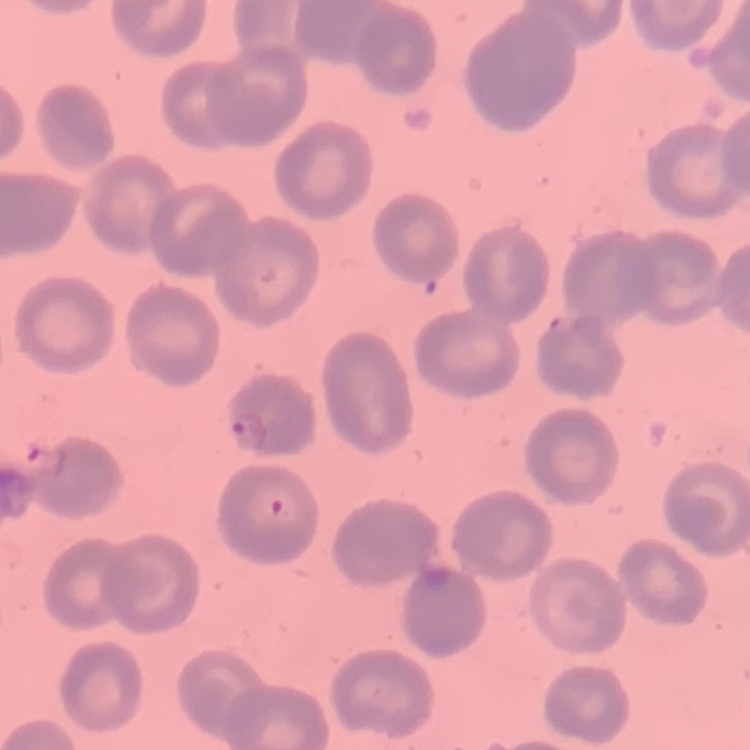
red blood cell morphology = no rouleaux formation
image type = one tile cut from a larger photomicrograph
stain = Field's or Giemsa
preparation = thin blood smear